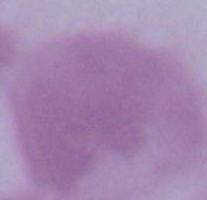

1000x magnification. Micrograph. An erythrocyte is seen.